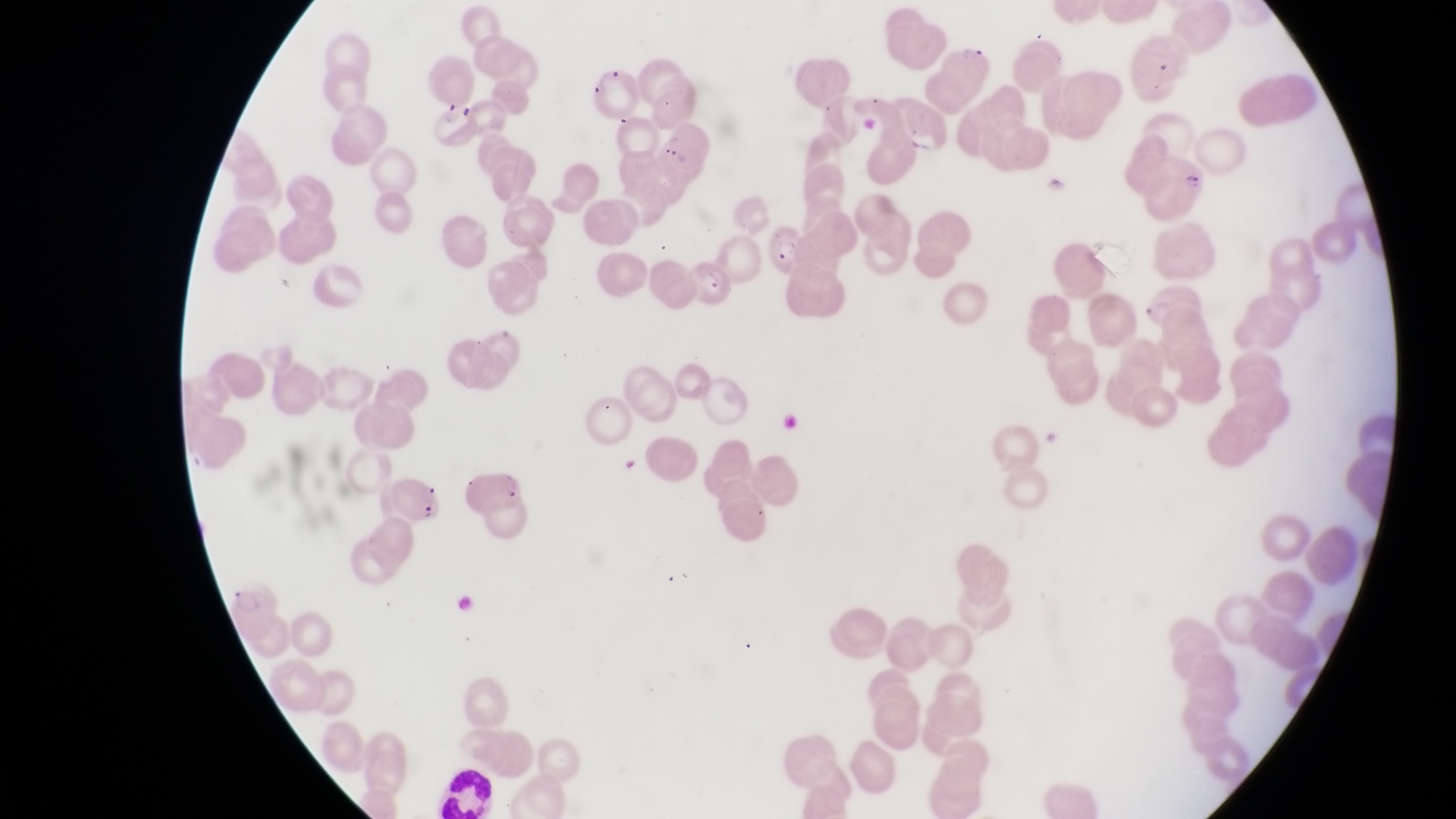
Approximate bounding boxes as [left, top, right, bottom] in pixels.
Summary:
  - Parasitised red blood cell locations: [948, 40, 1000, 99], [594, 61, 646, 120], [430, 93, 485, 148], [895, 96, 953, 162], [655, 126, 708, 176], [1149, 146, 1216, 222], [764, 219, 803, 272], [692, 256, 745, 315], [386, 472, 446, 527]
  - Leukocyte locations: [434, 759, 495, 817]
  - Image size: 1456×819 pixels
  - Field of view: single
  - Capture: smartphone photograph through the eyepiece of an Olympus CX-23 microscope
  - Country: Uganda
  - Magnification: 1000x
  - Preparation: thin blood smear